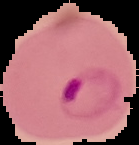 From a thin blood film. Segmented cell region on a black background. Result: Plasmodium parasites detected. Image is 139×145 pixels.